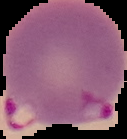 Image is 127×139 pixels. Result: Plasmodium parasites identified. Segmented cell region on a black background. From a thin blood smear.